Report the malaria status of this cell.
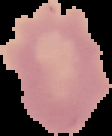

It is uninfected.

image size = 112×136 pixels
preparation = thin blood film
image type = segmented cell region on a black background